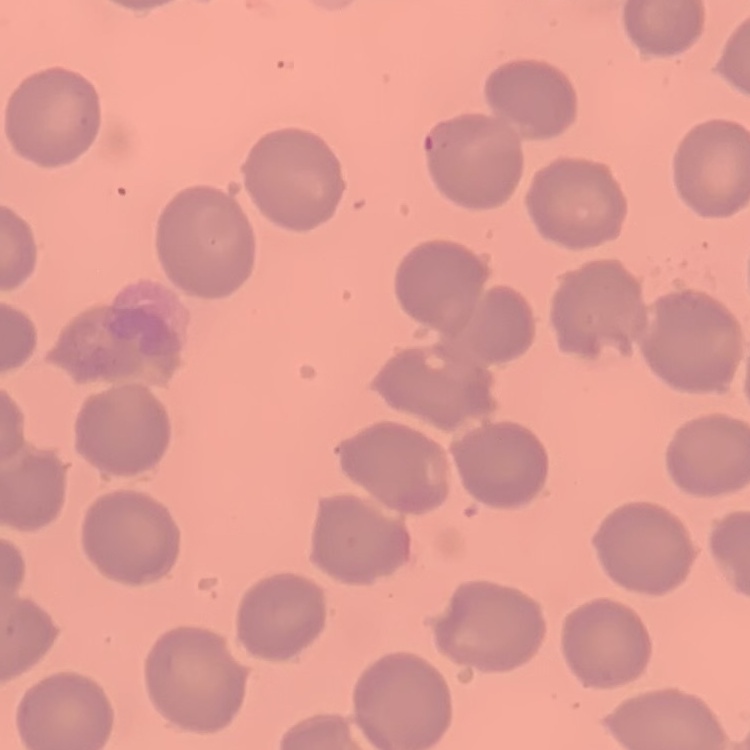
The erythrocytes show no rouleaux formation. Field's or Giemsa stain. Thin blood film. One tile cut from a larger photomicrograph.